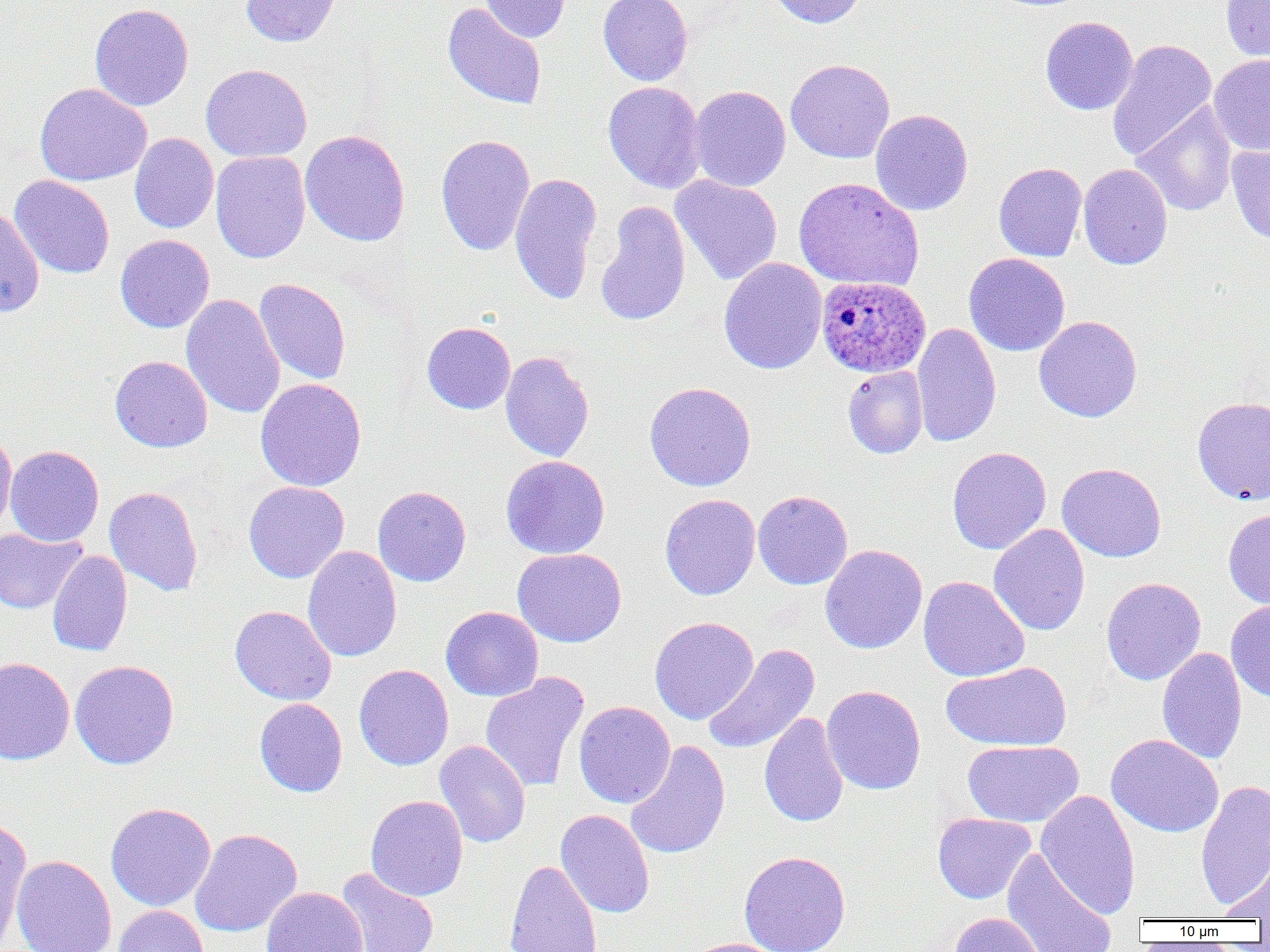

slide_level_diagnosis: Plasmodium ovale
preparation: thin blood film
image_size: 1270×952 pixels
magnification: 1000x
uninfected_red_blood_cell_locations: 'approximate bounding boxes as named x1/y1/x2/y2 corners in pixels: (x1=240, y1=0, x2=341, y2=47), (x1=480, y1=0, x2=571, y2=43), (x1=598, y1=0, x2=693, y2=86), (x1=768, y1=0, x2=867, y2=28), (x1=1220, y1=0, x2=1270, y2=64), (x1=442, y1=2, x2=547, y2=110), (x1=89, y1=3, x2=194, y2=111), (x1=1040, y1=16, x2=1138, y2=116), (x1=1106, y1=38, x2=1217, y2=162), (x1=1209, y1=54, x2=1270, y2=157), (x1=785, y1=58, x2=895, y2=164), (x1=201, y1=64, x2=312, y2=162), (x1=603, y1=81, x2=706, y2=194), (x1=34, y1=83, x2=152, y2=186), (x1=690, y1=85, x2=791, y2=191), (x1=1132, y1=101, x2=1238, y2=217), (x1=870, y1=109, x2=973, y2=216), (x1=1107, y1=120, x2=1207, y2=236), (x1=300, y1=129, x2=411, y2=247), (x1=130, y1=133, x2=219, y2=234), (x1=435, y1=133, x2=535, y2=256), (x1=1226, y1=143, x2=1270, y2=244), (x1=211, y1=151, x2=311, y2=264), (x1=993, y1=162, x2=1087, y2=262), (x1=1078, y1=163, x2=1172, y2=270), (x1=509, y1=172, x2=602, y2=305), (x1=9, y1=175, x2=115, y2=279), (x1=671, y1=175, x2=783, y2=285), (x1=794, y1=177, x2=924, y2=291), (x1=596, y1=200, x2=691, y2=327), (x1=0, y1=206, x2=45, y2=316), (x1=115, y1=235, x2=215, y2=333), (x1=963, y1=253, x2=1070, y2=356), (x1=718, y1=257, x2=827, y2=375), (x1=254, y1=278, x2=351, y2=385), (x1=181, y1=293, x2=285, y2=419), (x1=1034, y1=315, x2=1143, y2=422), (x1=422, y1=322, x2=516, y2=414), (x1=911, y1=322, x2=1001, y2=447), (x1=500, y1=351, x2=594, y2=462), (x1=109, y1=355, x2=213, y2=453), (x1=843, y1=366, x2=928, y2=459), (x1=255, y1=378, x2=367, y2=491), (x1=644, y1=381, x2=757, y2=492), (x1=1192, y1=396, x2=1270, y2=505), (x1=0, y1=429, x2=17, y2=539), (x1=5, y1=445, x2=104, y2=546), (x1=946, y1=446, x2=1051, y2=555), (x1=501, y1=455, x2=610, y2=559), (x1=1056, y1=462, x2=1167, y2=563), (x1=243, y1=481, x2=349, y2=583), (x1=372, y1=485, x2=472, y2=587), (x1=103, y1=486, x2=204, y2=596), (x1=753, y1=490, x2=853, y2=590), (x1=660, y1=494, x2=761, y2=600), (x1=1223, y1=508, x2=1270, y2=610), (x1=989, y1=524, x2=1090, y2=636), (x1=0, y1=527, x2=86, y2=614), (x1=820, y1=544, x2=927, y2=654), (x1=302, y1=545, x2=402, y2=662), (x1=512, y1=548, x2=627, y2=647), (x1=47, y1=550, x2=132, y2=657), (x1=918, y1=576, x2=1030, y2=682), (x1=1101, y1=577, x2=1206, y2=686), (x1=1225, y1=599, x2=1270, y2=701), (x1=229, y1=605, x2=337, y2=706), (x1=440, y1=606, x2=543, y2=701), (x1=649, y1=616, x2=759, y2=724), (x1=702, y1=644, x2=820, y2=755), (x1=1157, y1=647, x2=1247, y2=765), (x1=0, y1=656, x2=75, y2=766), (x1=69, y1=659, x2=179, y2=770), (x1=942, y1=661, x2=1072, y2=751), (x1=354, y1=664, x2=454, y2=771), (x1=480, y1=672, x2=589, y2=792), (x1=821, y1=685, x2=926, y2=795), (x1=254, y1=698, x2=348, y2=797), (x1=574, y1=701, x2=676, y2=809), (x1=759, y1=712, x2=849, y2=827), (x1=1105, y1=734, x2=1224, y2=838), (x1=434, y1=740, x2=531, y2=848), (x1=624, y1=740, x2=731, y2=860), (x1=963, y1=740, x2=1083, y2=827), (x1=1195, y1=779, x2=1270, y2=911), (x1=1036, y1=789, x2=1140, y2=919), (x1=366, y1=795, x2=468, y2=901), (x1=105, y1=802, x2=216, y2=911), (x1=555, y1=809, x2=655, y2=919), (x1=932, y1=812, x2=1036, y2=904), (x1=0, y1=815, x2=32, y2=946), (x1=189, y1=828, x2=302, y2=938), (x1=1002, y1=849, x2=1118, y2=952), (x1=738, y1=850, x2=851, y2=952), (x1=11, y1=855, x2=117, y2=952), (x1=1219, y1=856, x2=1270, y2=921), (x1=504, y1=858, x2=603, y2=952), (x1=334, y1=867, x2=439, y2=952), (x1=260, y1=886, x2=368, y2=952), (x1=112, y1=905, x2=210, y2=952), (x1=949, y1=912, x2=1046, y2=952), (x1=679, y1=938, x2=790, y2=952)'
field_of_view: single
plasmodium_ovale_infected_red_blood_cell_locations: 'approximate bounding boxes as named x1/y1/x2/y2 corners in pixels: (x1=816, y1=275, x2=931, y2=378)'
modality: optical microscopy